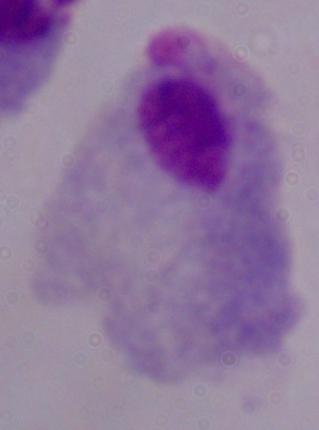
Photomicrograph. A trichomonad is shown. 1000x magnification.